Name the parasite shown.
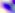
This is Toxoplasma gondii.

Summary:
  - Modality: micrograph
  - Magnification: 400x